Identify the parasite.
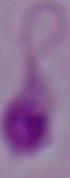

This is Leishmania.

Micrograph. 1000x magnification.